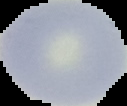
{
  "malaria_status": "uninfected",
  "image_size": "127×106 pixels",
  "preparation": "thin blood smear",
  "image_type": "cell region segmented out of the field of view; surrounding area masked to black"
}